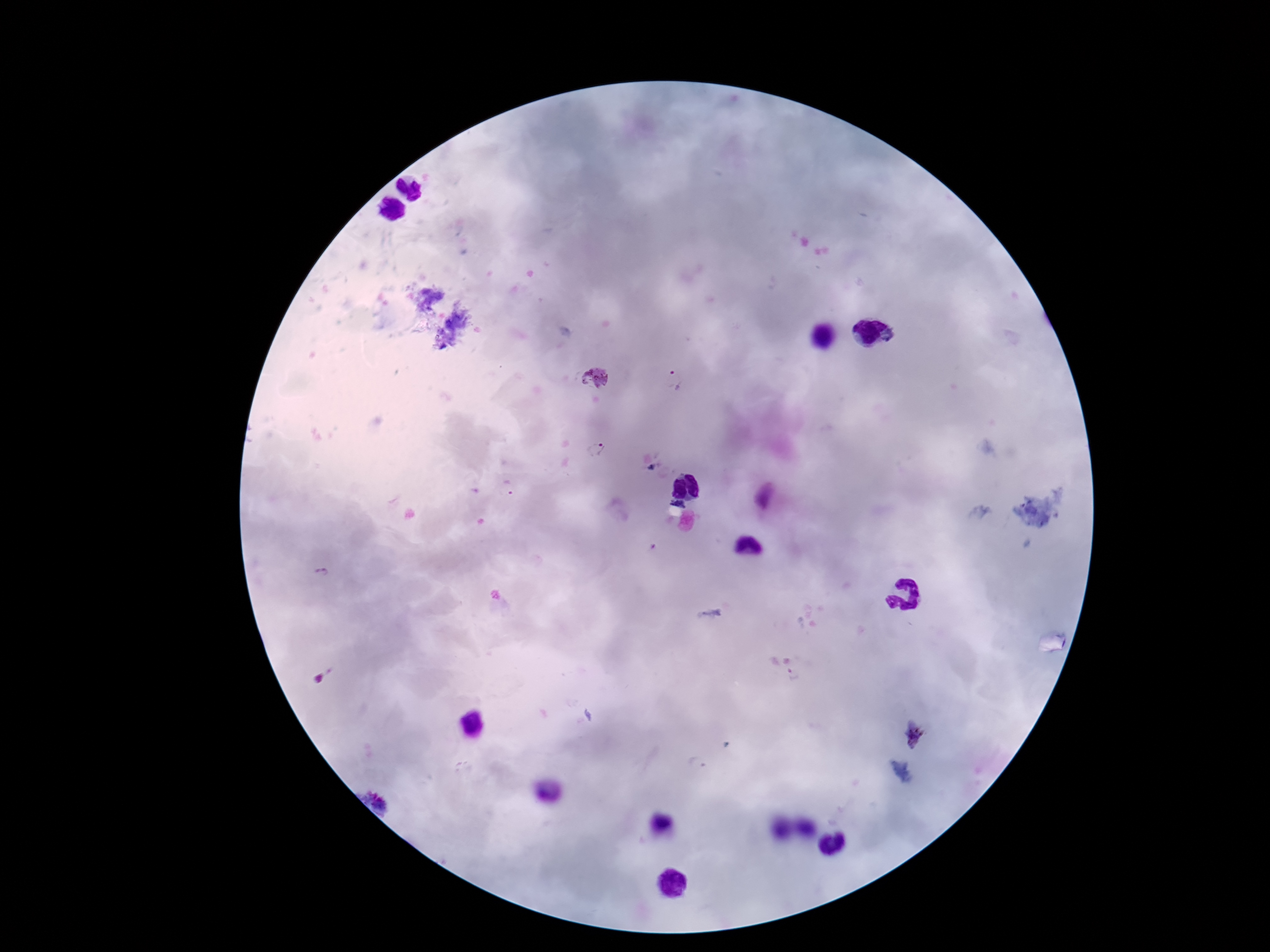

Approximate centers as {x, y} in pixels.
Summary:
  - Plasmodium parasite locations: {595, 377}, {675, 382}, {591, 449}, {509, 490}, {322, 574}, {793, 676}, {913, 736}
  - Stain: Giemsa
  - Field of view: single
  - Magnification: 100x
  - Patient malaria status: positive
  - Image size: 1270×952 pixels
  - Preparation: thick blood film
  - Capture: smartphone camera through the microscope eyepiece